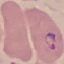
{
  "malaria_status": "parasitized",
  "image_type": "cell patch, automatically extracted from a larger field of view and resized to 64 × 64 pixels",
  "capture": "smartphone camera at the microscope eyepiece",
  "stain": "Giemsa",
  "preparation": "thin blood smear"
}